Locate and identify every blood parasite.
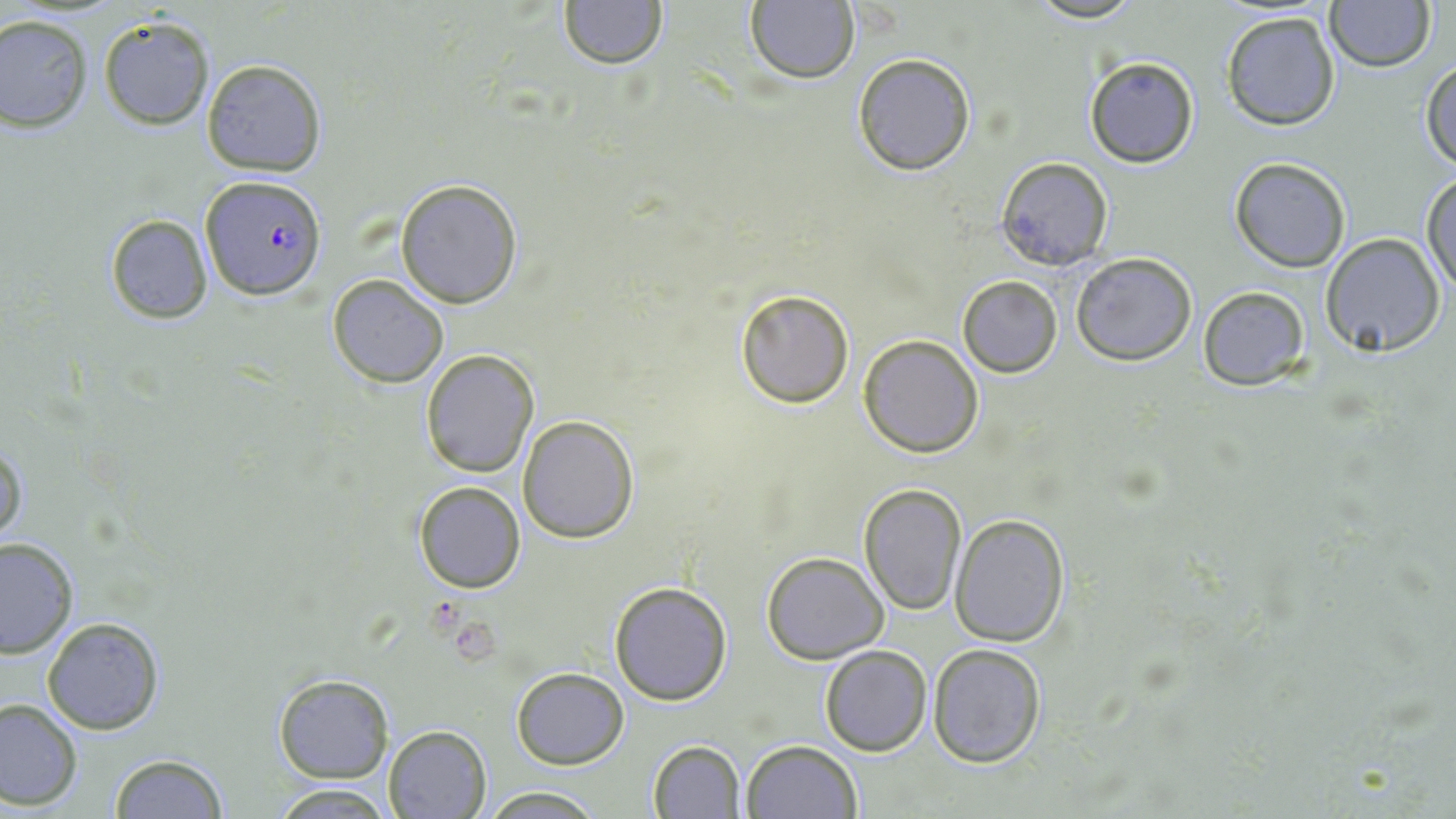
Approximate bounding boxes as named x1/y1/x2/y2 corners in pixels.
Plasmodium falciparum-infected red blood cells: (x1=200, y1=176, x2=327, y2=301).
No Plasmodium ovale, Plasmodium malariae, Plasmodium vivax, Babesia divergens, or Trypanosoma brucei observed.

Summary:
  - Uninfected red blood cell locations: (x1=558, y1=0, x2=667, y2=70), (x1=1021, y1=0, x2=1153, y2=25), (x1=744, y1=1, x2=860, y2=86), (x1=1323, y1=1, x2=1434, y2=73), (x1=1219, y1=10, x2=1341, y2=131), (x1=0, y1=14, x2=93, y2=131), (x1=98, y1=15, x2=214, y2=130), (x1=851, y1=52, x2=977, y2=176), (x1=1084, y1=56, x2=1200, y2=168), (x1=201, y1=59, x2=326, y2=175), (x1=1421, y1=59, x2=1456, y2=168), (x1=994, y1=156, x2=1114, y2=271), (x1=1230, y1=157, x2=1350, y2=273), (x1=1423, y1=173, x2=1455, y2=298), (x1=395, y1=180, x2=522, y2=309), (x1=105, y1=214, x2=212, y2=323), (x1=1319, y1=233, x2=1445, y2=357), (x1=1070, y1=251, x2=1199, y2=367), (x1=327, y1=275, x2=448, y2=389), (x1=955, y1=276, x2=1063, y2=378), (x1=734, y1=286, x2=855, y2=408), (x1=1197, y1=286, x2=1310, y2=389), (x1=858, y1=335, x2=984, y2=458), (x1=421, y1=350, x2=539, y2=477), (x1=517, y1=415, x2=639, y2=542), (x1=1, y1=440, x2=28, y2=553), (x1=412, y1=481, x2=525, y2=593), (x1=860, y1=482, x2=968, y2=616), (x1=949, y1=513, x2=1069, y2=647), (x1=0, y1=538, x2=77, y2=659), (x1=760, y1=550, x2=888, y2=663), (x1=608, y1=580, x2=733, y2=704), (x1=43, y1=616, x2=164, y2=734), (x1=928, y1=644, x2=1047, y2=768), (x1=820, y1=645, x2=933, y2=756), (x1=511, y1=667, x2=628, y2=768), (x1=272, y1=674, x2=394, y2=783), (x1=0, y1=698, x2=82, y2=810), (x1=384, y1=724, x2=493, y2=818), (x1=646, y1=739, x2=745, y2=818), (x1=741, y1=740, x2=861, y2=819), (x1=108, y1=752, x2=230, y2=819), (x1=270, y1=785, x2=400, y2=818), (x1=480, y1=786, x2=607, y2=818)
  - Slide-level diagnosis: Plasmodium falciparum
  - Stain: May-Grünwald-Giemsa
  - Preparation: thin blood smear
  - Modality: optical microscopy
  - Magnification: 1000x
  - Image size: 1456×819 pixels
  - Field of view: single